Identify the parasite.
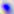

Toxoplasma gondii.

modality = micrograph
magnification = 400x